Describe the morphology of the erythrocytes.
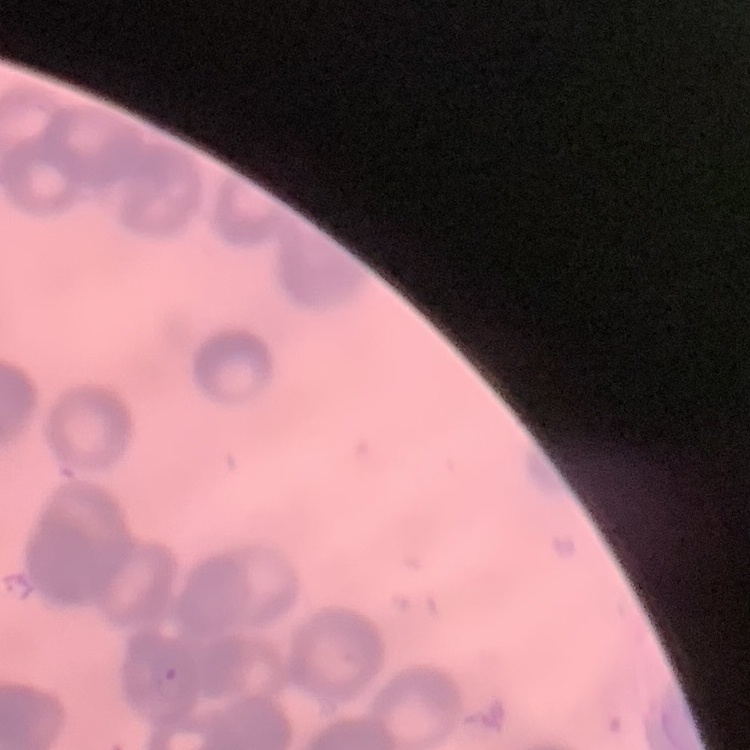

They show rouleaux formation.

Summary:
  - Stain: Field's or Giemsa
  - Preparation: thin blood film
  - Image type: square crop of a larger photomicrograph